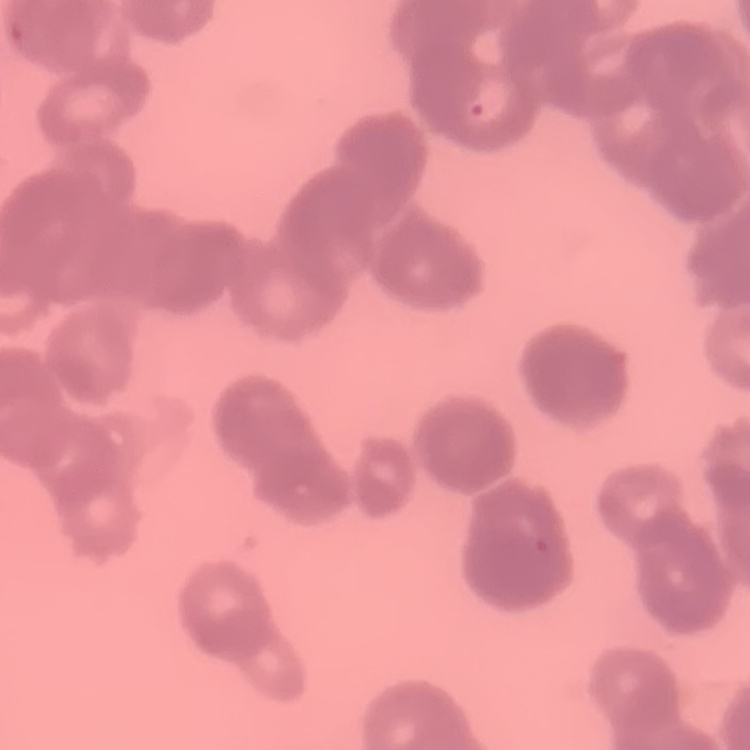 The red blood cells show rouleaux formation. Stained with either Field's or Giemsa. Thin blood smear. Square crop of a larger photomicrograph.